Locate every blood parasite and identify its species.
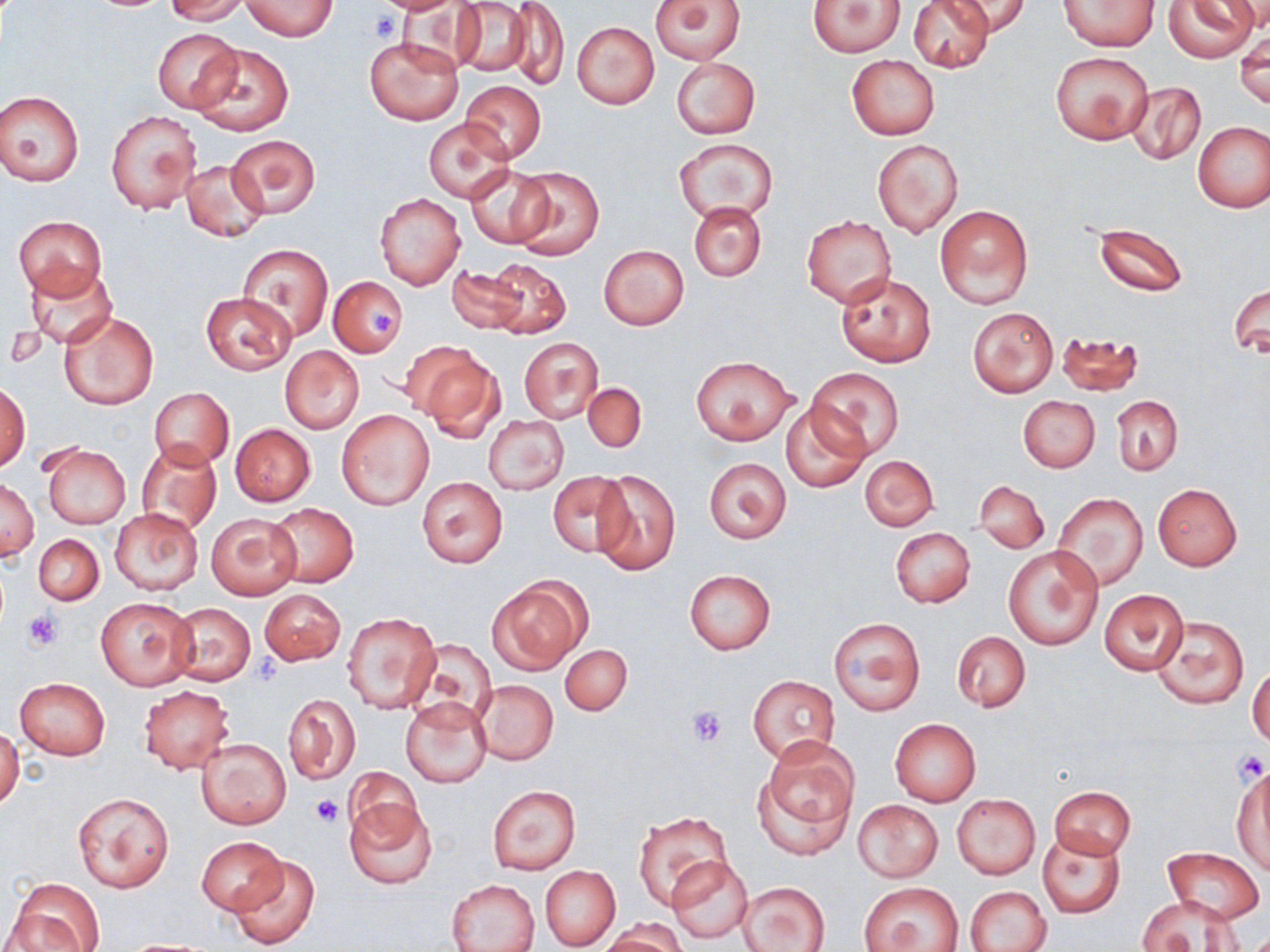

No blood parasites seen.

slide_level_diagnosis: no evidence of blood parasites
platelet_locations: 'approximate bounding boxes as named x1/y1/x2/y2 corners in pixels: (x1=369, y1=10, x2=404, y2=45), (x1=365, y1=307, x2=398, y2=336), (x1=23, y1=610, x2=63, y2=651), (x1=686, y1=706, x2=727, y2=747), (x1=1231, y1=749, x2=1269, y2=786), (x1=310, y1=795, x2=346, y2=828)'
modality: light microscopy
stain: May-Grünwald-Giemsa
image_size: 1270×952 pixels
magnification: 1000x
preparation: thin blood smear
uninfected_red_blood_cell_locations: 'approximate bounding boxes as named x1/y1/x2/y2 corners in pixels: (x1=163, y1=0, x2=252, y2=24), (x1=649, y1=0, x2=746, y2=65), (x1=907, y1=0, x2=993, y2=73), (x1=946, y1=0, x2=1030, y2=37), (x1=1163, y1=0, x2=1256, y2=61), (x1=242, y1=1, x2=337, y2=40), (x1=450, y1=1, x2=535, y2=79), (x1=506, y1=1, x2=570, y2=93), (x1=807, y1=1, x2=904, y2=56), (x1=1057, y1=1, x2=1158, y2=51), (x1=1225, y1=2, x2=1270, y2=36), (x1=572, y1=22, x2=659, y2=108), (x1=153, y1=28, x2=242, y2=111), (x1=1236, y1=35, x2=1269, y2=108), (x1=365, y1=36, x2=463, y2=125), (x1=194, y1=41, x2=294, y2=136), (x1=1051, y1=52, x2=1154, y2=146), (x1=846, y1=55, x2=939, y2=140), (x1=671, y1=58, x2=760, y2=137), (x1=1126, y1=80, x2=1206, y2=166), (x1=461, y1=81, x2=546, y2=162), (x1=0, y1=90, x2=84, y2=186), (x1=106, y1=110, x2=200, y2=214), (x1=423, y1=119, x2=514, y2=201), (x1=1193, y1=121, x2=1270, y2=212), (x1=227, y1=135, x2=319, y2=216), (x1=674, y1=138, x2=777, y2=223), (x1=872, y1=139, x2=963, y2=237), (x1=181, y1=159, x2=268, y2=241), (x1=467, y1=165, x2=553, y2=248), (x1=510, y1=167, x2=604, y2=259), (x1=376, y1=193, x2=464, y2=289), (x1=689, y1=203, x2=766, y2=282), (x1=934, y1=204, x2=1034, y2=310), (x1=802, y1=215, x2=897, y2=308), (x1=13, y1=216, x2=106, y2=297), (x1=1094, y1=223, x2=1187, y2=296), (x1=239, y1=243, x2=332, y2=341), (x1=599, y1=245, x2=689, y2=329), (x1=485, y1=258, x2=571, y2=339), (x1=24, y1=264, x2=119, y2=349), (x1=448, y1=265, x2=528, y2=335), (x1=837, y1=273, x2=937, y2=366), (x1=329, y1=276, x2=408, y2=356), (x1=1230, y1=282, x2=1269, y2=360), (x1=201, y1=293, x2=297, y2=375), (x1=969, y1=308, x2=1058, y2=395), (x1=59, y1=311, x2=157, y2=410), (x1=1057, y1=331, x2=1144, y2=397), (x1=519, y1=338, x2=603, y2=423), (x1=280, y1=345, x2=364, y2=433), (x1=411, y1=346, x2=504, y2=439), (x1=691, y1=355, x2=796, y2=444), (x1=806, y1=369, x2=905, y2=461), (x1=583, y1=382, x2=646, y2=453), (x1=0, y1=383, x2=30, y2=471), (x1=150, y1=388, x2=234, y2=468), (x1=1018, y1=396, x2=1100, y2=472), (x1=1113, y1=396, x2=1183, y2=475), (x1=781, y1=402, x2=870, y2=492), (x1=338, y1=410, x2=434, y2=510), (x1=483, y1=415, x2=568, y2=494), (x1=230, y1=424, x2=315, y2=506), (x1=135, y1=441, x2=223, y2=534), (x1=41, y1=443, x2=130, y2=528), (x1=860, y1=454, x2=939, y2=532), (x1=703, y1=457, x2=792, y2=544), (x1=590, y1=470, x2=681, y2=577), (x1=545, y1=471, x2=632, y2=556), (x1=417, y1=477, x2=507, y2=567), (x1=1, y1=479, x2=38, y2=559), (x1=975, y1=480, x2=1049, y2=552), (x1=1152, y1=484, x2=1241, y2=570), (x1=1053, y1=493, x2=1148, y2=590), (x1=267, y1=504, x2=359, y2=588), (x1=110, y1=508, x2=202, y2=595), (x1=207, y1=513, x2=301, y2=600), (x1=1023, y1=517, x2=1138, y2=629), (x1=890, y1=528, x2=975, y2=608), (x1=34, y1=534, x2=103, y2=605), (x1=1003, y1=545, x2=1103, y2=650), (x1=684, y1=569, x2=776, y2=654), (x1=487, y1=581, x2=587, y2=674), (x1=258, y1=588, x2=345, y2=665), (x1=1100, y1=590, x2=1188, y2=675), (x1=96, y1=597, x2=197, y2=689), (x1=169, y1=602, x2=256, y2=685), (x1=342, y1=612, x2=439, y2=713), (x1=1151, y1=615, x2=1248, y2=709), (x1=829, y1=617, x2=925, y2=715), (x1=952, y1=630, x2=1031, y2=712), (x1=409, y1=640, x2=496, y2=722), (x1=561, y1=644, x2=632, y2=716), (x1=1248, y1=664, x2=1270, y2=747), (x1=749, y1=674, x2=840, y2=765), (x1=14, y1=678, x2=110, y2=760), (x1=473, y1=679, x2=557, y2=764), (x1=138, y1=686, x2=234, y2=772), (x1=282, y1=692, x2=360, y2=786), (x1=402, y1=698, x2=492, y2=787), (x1=890, y1=719, x2=981, y2=805), (x1=0, y1=726, x2=23, y2=811), (x1=195, y1=736, x2=292, y2=829), (x1=754, y1=737, x2=859, y2=857), (x1=1232, y1=764, x2=1270, y2=873), (x1=344, y1=768, x2=425, y2=857), (x1=487, y1=785, x2=581, y2=873), (x1=1050, y1=787, x2=1135, y2=858), (x1=72, y1=792, x2=173, y2=892), (x1=952, y1=794, x2=1041, y2=879), (x1=344, y1=797, x2=439, y2=890), (x1=852, y1=799, x2=943, y2=881), (x1=634, y1=811, x2=734, y2=907), (x1=1038, y1=832, x2=1125, y2=918), (x1=196, y1=836, x2=285, y2=914), (x1=1163, y1=847, x2=1265, y2=924), (x1=229, y1=853, x2=319, y2=950), (x1=665, y1=856, x2=755, y2=945), (x1=540, y1=866, x2=620, y2=950), (x1=8, y1=879, x2=104, y2=949), (x1=448, y1=879, x2=540, y2=952), (x1=738, y1=882, x2=830, y2=951), (x1=861, y1=883, x2=962, y2=951), (x1=966, y1=887, x2=1051, y2=952), (x1=1138, y1=894, x2=1243, y2=952), (x1=603, y1=921, x2=686, y2=951)'
field_of_view: single